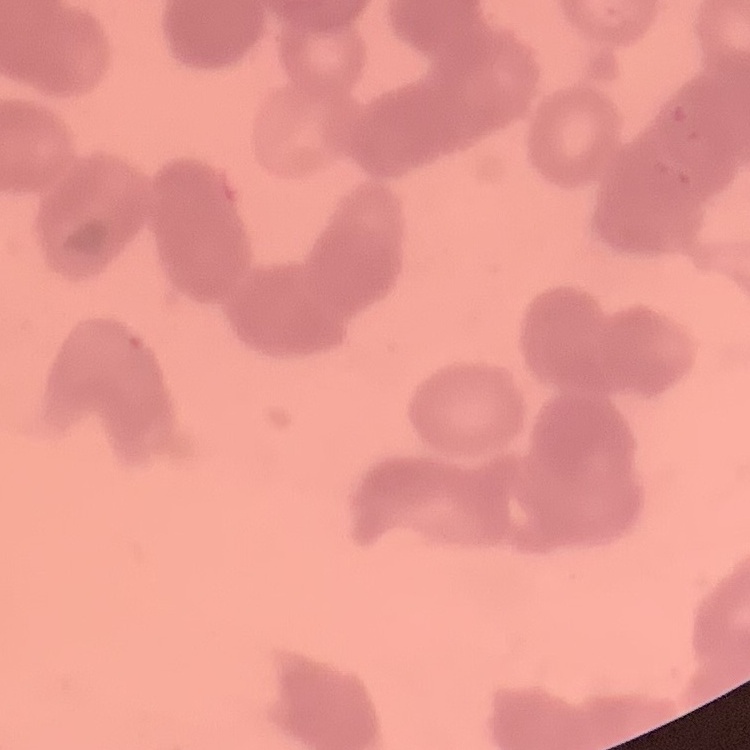
erythrocyte morphology = rouleaux formation
stain = Field's or Giemsa
image type = one tile cut from a larger photomicrograph
preparation = thin blood smear